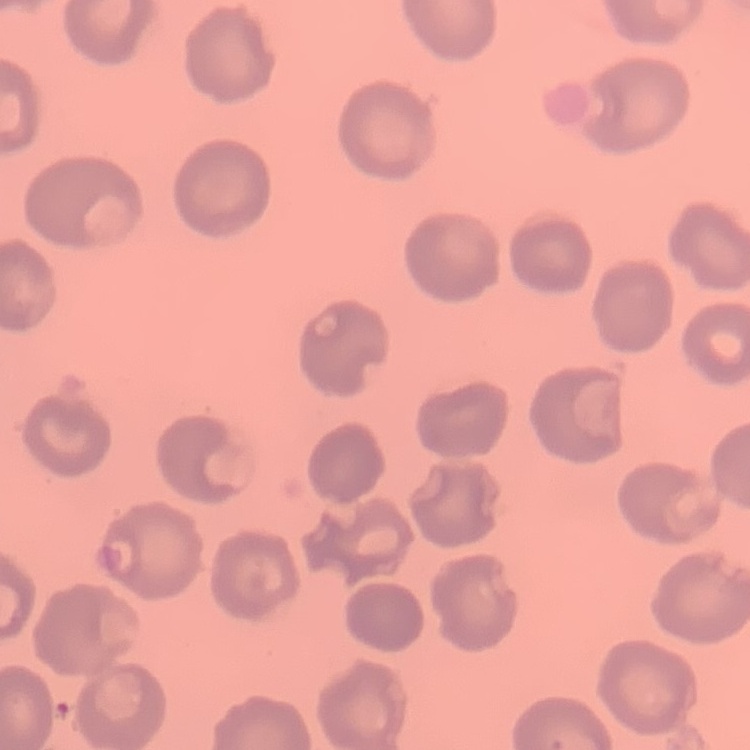
Summary:
  - Red blood cell morphology: no rouleaux formation
  - Preparation: thin blood smear
  - Stain: Field's or Giemsa
  - Image type: one tile cut from a larger photomicrograph